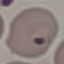
result = malaria parasites identified
capture = smartphone camera at the microscope eyepiece
image type = cell patch, automatically extracted from a larger field of view and resized to 64 × 64 pixels
preparation = thin blood smear
stain = Giemsa